Assess this cell for malaria.
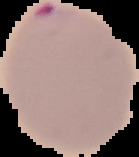

Parasitized.

Summary:
  - Image size: 139×157 pixels
  - Preparation: thin blood film
  - Image type: segmented cell region with the area outside set to black